Outline each uninfected red blood cell.
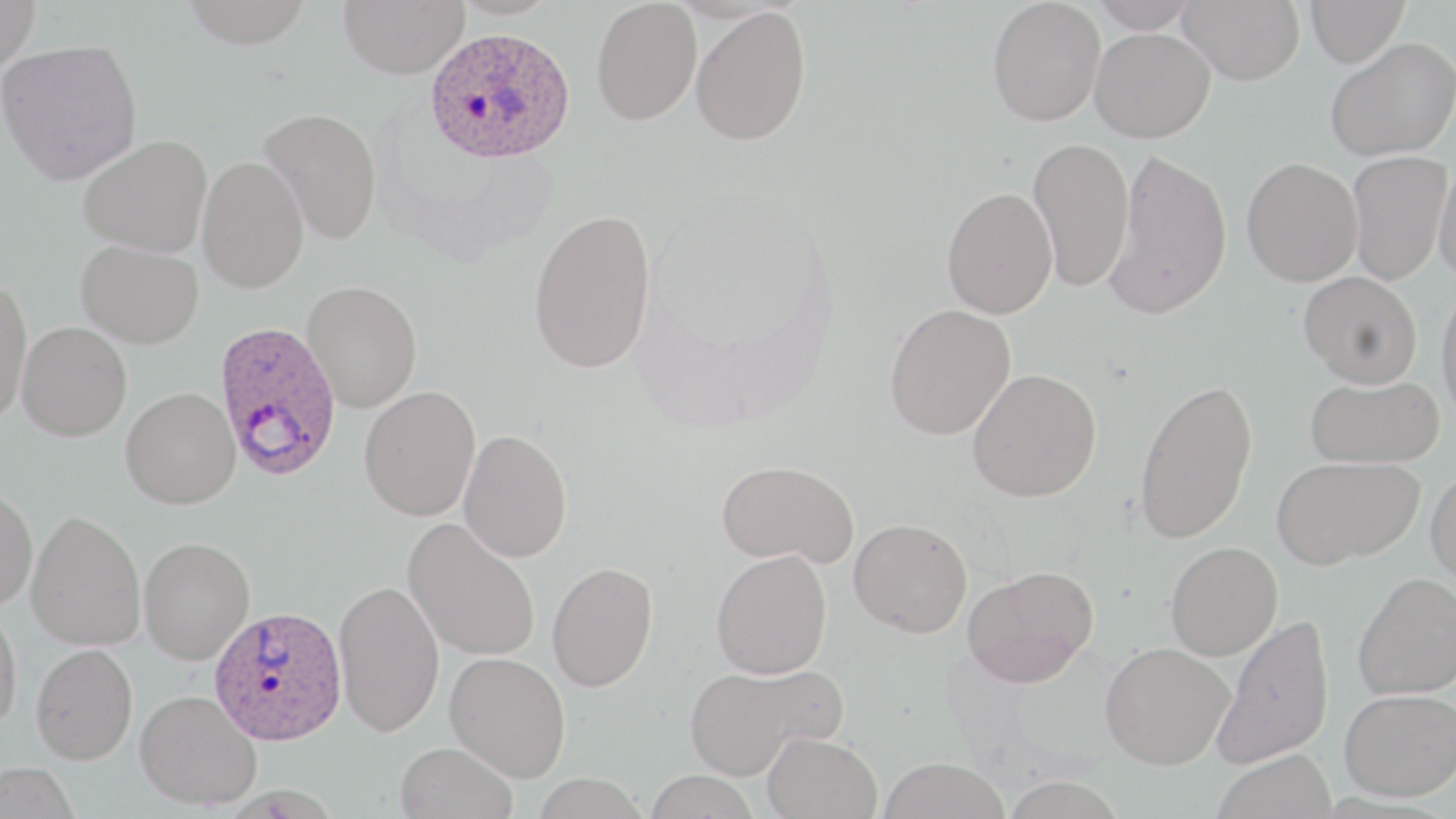
Approximate bounding boxes as (x1,y1)-(x2,y2) corner pairs in pixels.
Uninfected red blood cells: (0,0)-(40,72), (181,0)-(314,48), (338,0)-(469,78), (449,0)-(563,19), (987,0)-(1106,125), (1090,0)-(1200,33), (1176,0)-(1304,84), (1305,0)-(1410,67), (591,1)-(702,125), (691,6)-(812,145), (1090,27)-(1216,142), (1325,37)-(1455,161), (0,39)-(142,185), (258,107)-(383,244), (79,135)-(211,257), (1028,137)-(1134,292), (1105,149)-(1232,319), (1346,149)-(1451,286), (197,155)-(309,293), (1432,155)-(1456,286), (1241,158)-(1363,286), (942,187)-(1058,318), (528,208)-(656,374), (77,240)-(204,348), (1299,271)-(1422,387), (0,277)-(31,427), (1436,279)-(1456,424), (303,280)-(422,412), (884,303)-(1016,440), (17,322)-(132,441), (967,368)-(1101,502), (1305,374)-(1445,468), (1133,377)-(1258,544), (359,385)-(481,520), (120,387)-(241,509), (459,429)-(573,562), (1272,455)-(1424,569), (716,459)-(859,566), (1426,467)-(1456,593), (0,485)-(38,610), (26,510)-(146,651), (403,518)-(541,661), (849,518)-(972,637), (138,536)-(255,665), (1165,541)-(1283,660), (711,549)-(832,678), (547,562)-(658,692), (963,565)-(1098,688), (1353,572)-(1456,700), (334,580)-(445,737), (0,602)-(23,732), (1213,612)-(1334,769), (1099,642)-(1234,769), (31,643)-(137,763), (445,651)-(571,781), (684,663)-(842,778), (1339,688)-(1456,801), (135,689)-(262,809), (762,731)-(883,819), (395,741)-(518,819), (1212,748)-(1337,818), (877,757)-(1009,819), (0,761)-(80,819), (644,770)-(761,819).

slide_level_diagnosis: Plasmodium ovale
modality: optical microscopy
image_size: 1456×819 pixels
field_of_view: single
stain: May-Grünwald-Giemsa
preparation: thin blood smear
magnification: 1000x
plasmodium_ovale_infected_red_blood_cell_locations: 'approximate bounding boxes as (x1,y1)-(x2,y2) corner pairs in pixels: (425,26)-(576,163), (213,320)-(343,481), (211,607)-(349,747)'